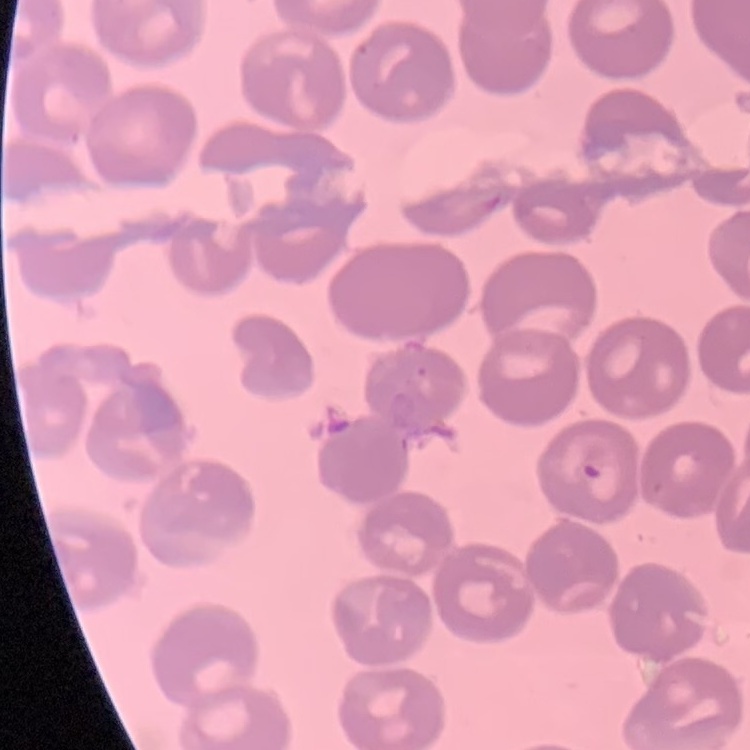

{
  "erythrocyte_morphology": "no rouleaux formation",
  "preparation": "thin blood smear",
  "stain": "Field's or Giemsa",
  "image_type": "square crop of a larger photomicrograph"
}